Comment on the morphology of the erythrocytes.
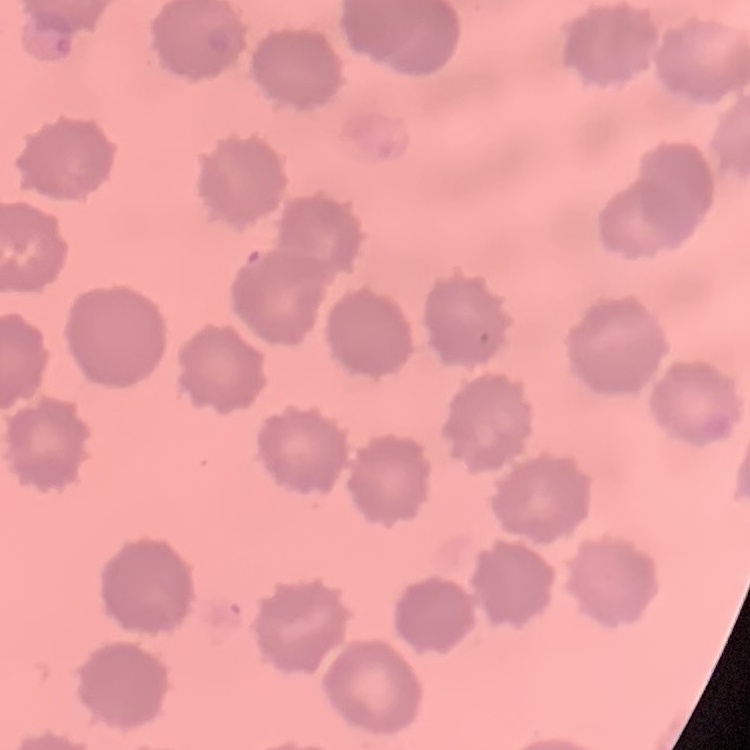

They show no rouleaux formation.

image type = square crop of a larger photomicrograph
preparation = thin peripheral smear
stain = Field's or Giemsa